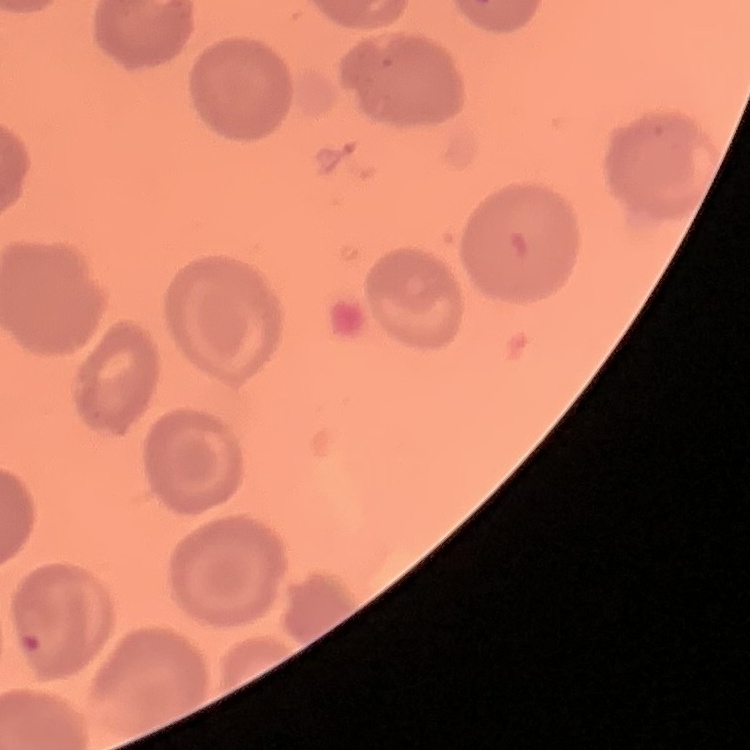
Summary:
  - Red blood cell morphology: no rouleaux formation
  - Stain: Field's or Giemsa
  - Image type: square crop of a larger photomicrograph
  - Preparation: thin peripheral smear